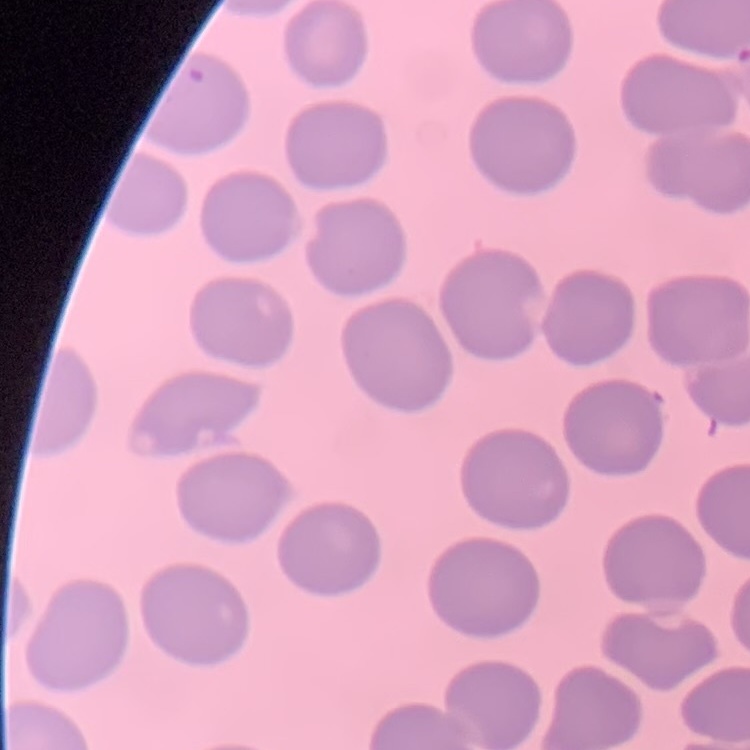
Summary:
  - Erythrocyte morphology: no rouleaux formation
  - Stain: Field's or Giemsa
  - Image type: one tile cut from a larger photomicrograph
  - Preparation: thin peripheral smear